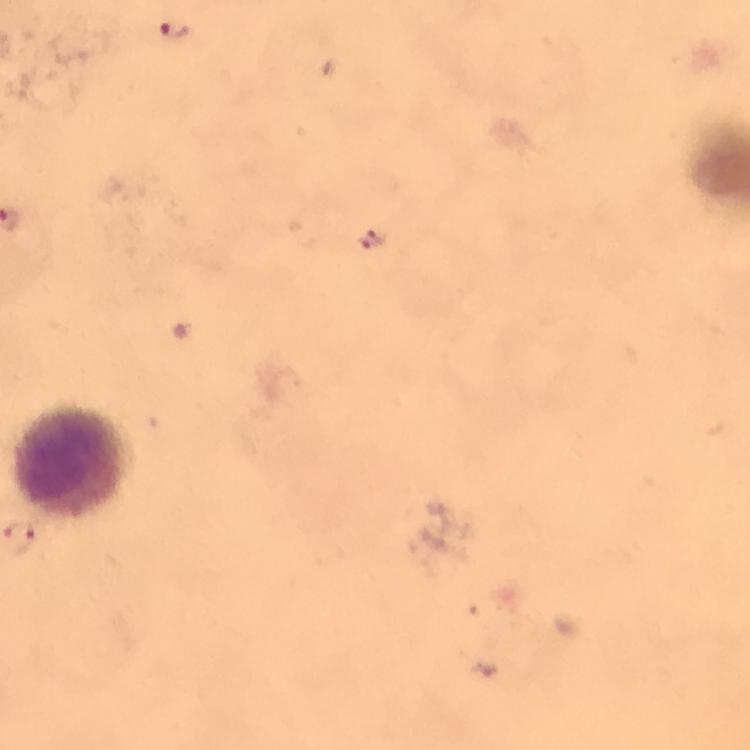
cropped_from: a single field of view
capture: smartphone mounted on the microscope
immersion_oil: applied
preparation: thick blood smear
plasmodium_parasite_locations: 'approximate centers as {x, y} in pixels: {173, 33}, {373, 238}, {29, 540}'
magnification: 100x
context: from a diagnostic examination for malaria
image_size: 750×750 pixels
stain: Giemsa
leukocyte_locations: 'approximate centers as {x, y} in pixels: {75, 462}'